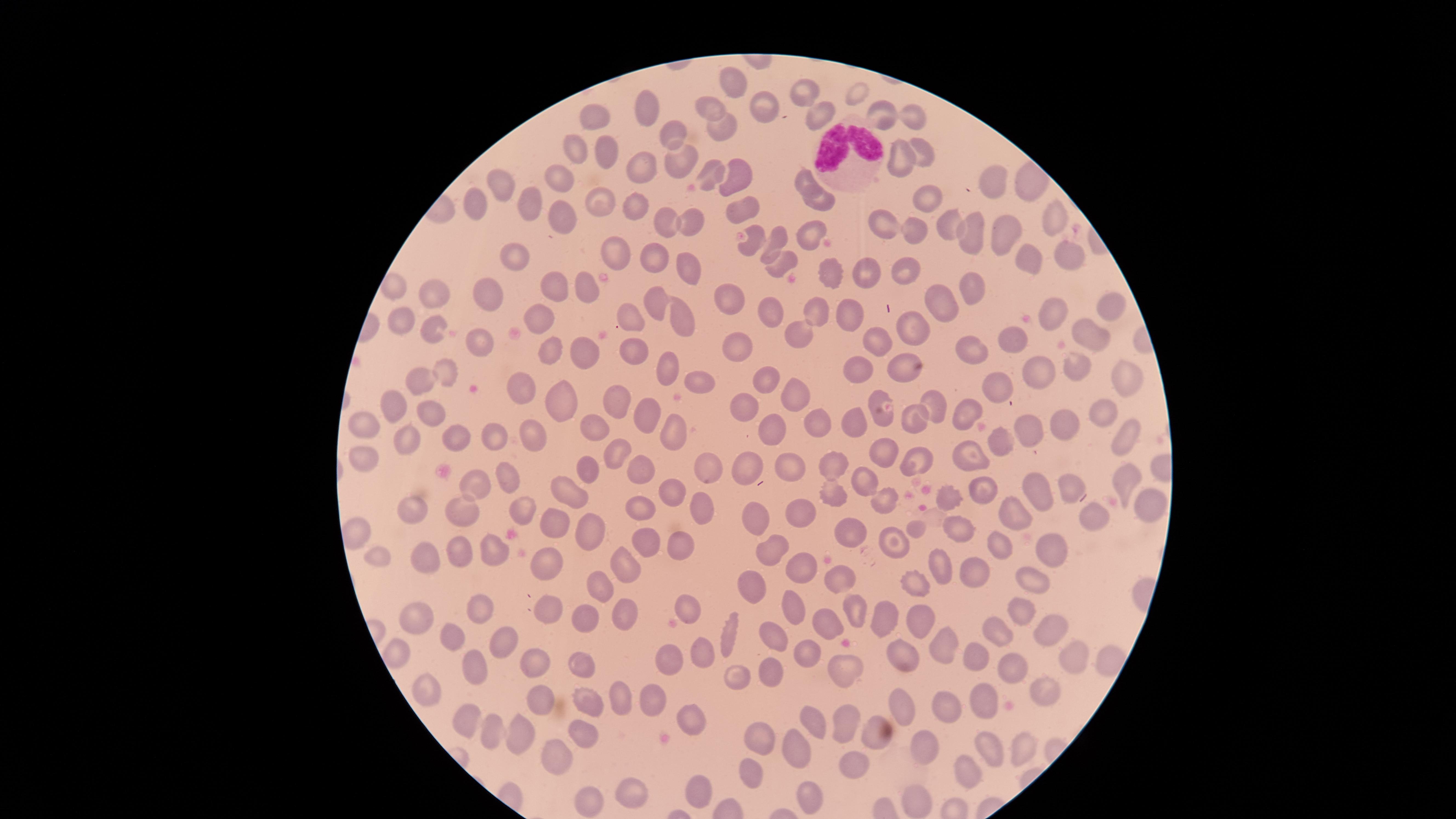
{
  "white_blood_cells": "approximate marker points as (x, y) in pixels: (848, 155)",
  "visible_region": "circular",
  "stain": "Giemsa",
  "image_size": "1456×819 pixels",
  "preparation": "thin smear of blood",
  "presence": "no malaria parasites detected",
  "uninfected_red_blood_cells": "approximate marker points as (x, y) in pixels: (733, 78), (805, 88), (859, 92), (649, 108), (766, 108), (714, 109), (588, 114), (916, 115), (814, 116), (880, 116), (722, 123), (671, 137), (605, 151), (579, 152), (899, 156), (921, 156), (678, 161), (646, 170), (715, 174), (738, 176), (995, 179), (802, 180), (565, 181), (502, 186), (600, 200), (926, 201), (526, 203), (823, 203), (743, 204), (474, 209), (633, 212), (688, 219), (1052, 219), (567, 220), (666, 223), (884, 227), (810, 229), (955, 229), (915, 233), (752, 238), (1003, 239), (777, 240), (973, 242), (617, 257), (1032, 258), (1073, 259), (654, 261), (513, 262), (784, 263), (695, 268), (826, 272), (906, 272), (867, 274), (551, 285), (970, 288), (390, 290), (590, 290), (435, 292), (724, 296), (485, 299), (942, 304), (658, 305), (769, 305), (1109, 310), (630, 312), (1057, 313), (848, 314), (816, 315), (541, 318), (682, 318), (400, 322), (430, 330), (911, 330), (797, 333), (1099, 341), (875, 342), (1009, 343), (482, 344), (969, 346), (734, 348), (632, 349), (551, 355), (591, 357), (1076, 367), (449, 368), (667, 369), (905, 370), (1044, 372), (860, 374), (1128, 380), (698, 381), (423, 382), (773, 386), (1003, 388), (520, 392), (792, 393), (748, 398), (876, 399), (566, 400), (616, 400), (400, 406), (1104, 407), (933, 408), (431, 411), (969, 413), (648, 415), (816, 420), (364, 424), (854, 424), (914, 424), (1066, 424), (592, 426), (1029, 426), (676, 430), (1125, 431), (452, 432), (770, 432), (493, 436), (408, 438), (999, 439), (540, 442), (616, 449), (883, 451), (364, 453), (970, 454), (917, 460), (746, 464), (835, 465), (787, 466), (707, 468), (584, 469), (641, 470), (509, 475), (1120, 476), (475, 478), (866, 478), (1072, 485), (985, 486), (569, 490), (670, 492), (1040, 492), (831, 494), (955, 500), (883, 503), (699, 504), (416, 508), (1146, 508), (521, 511), (641, 511), (801, 511), (463, 513), (757, 513), (555, 516), (1015, 518), (1099, 523), (848, 529), (919, 531), (956, 531), (584, 532), (648, 542), (893, 543), (683, 545), (1004, 549), (491, 550), (1053, 550), (766, 552), (458, 554), (379, 555), (425, 555), (629, 566), (549, 567), (800, 567), (941, 567), (969, 573), (837, 577), (1032, 579), (604, 582), (753, 584), (913, 584), (791, 604), (683, 606), (480, 611), (1021, 614), (549, 615), (853, 616), (882, 617), (627, 619), (589, 622), (916, 624), (418, 625), (831, 628), (1042, 632), (994, 633), (733, 635), (774, 636), (455, 640), (505, 640), (944, 643), (806, 651), (903, 653), (674, 654), (704, 654), (1068, 654), (983, 661), (535, 664), (574, 664), (1009, 664), (478, 669), (768, 671), (843, 671), (731, 678), (421, 688), (1050, 691), (621, 693), (647, 697), (535, 700), (584, 700), (982, 702), (940, 705), (904, 707), (694, 713), (469, 719), (813, 721), (843, 721), (491, 731), (872, 731), (522, 735), (584, 736), (763, 736), (1024, 746), (928, 748), (799, 750), (991, 753), (563, 764), (859, 765), (752, 769), (970, 777), (702, 780), (636, 789), (809, 797), (596, 801), (915, 803)",
  "field_of_view": "single",
  "capture": "smartphone photograph through the microscope eyepiece"
}